Assess this cell for malaria.
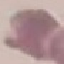

It is uninfected.

stain = Giemsa
capture = smartphone through the microscope eyepiece
preparation = thin blood smear
image type = automatically extracted cell patch, resized to 64 × 64 pixels